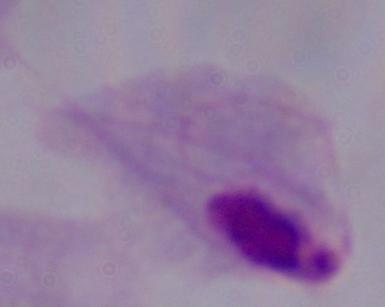
Summary:
  - Identification: trichomonad
  - Magnification: 1000x
  - Modality: micrograph